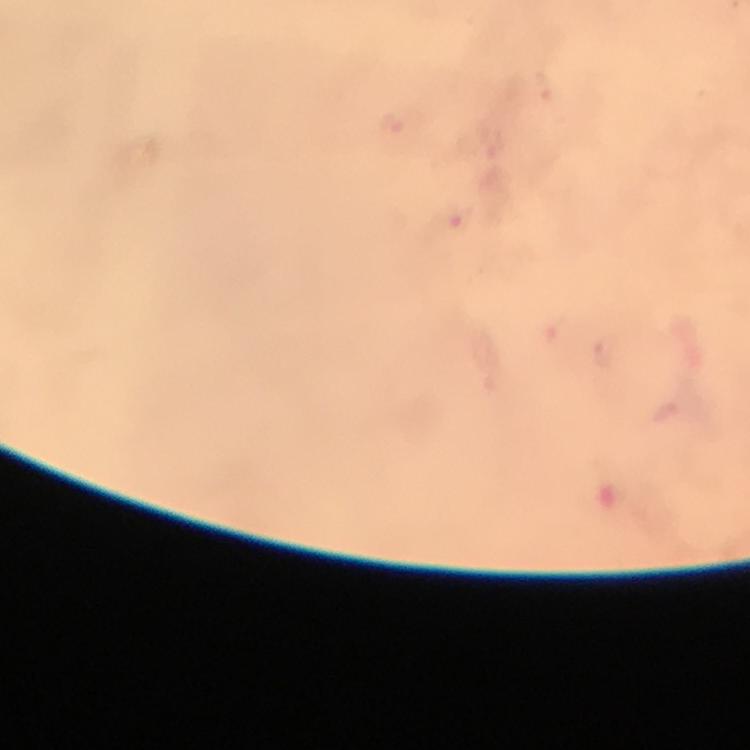
Approximate centers as {x, y} in pixels. Malaria parasite locations: {392, 125}, {454, 218}. Giemsa-stained preparation. Photographed through the microscope with a smartphone camera. Thick smear. Immersion oil was used. 100x magnification. Image is 750×750 pixels. A crop from one field of view. From a diagnostic examination for malaria.